Assess this cell for malaria.
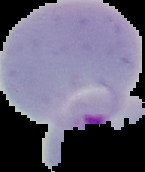
Parasitized.

Image is 145×172 pixels. The area outside the segmented cell region is set to black. From a thin blood film.